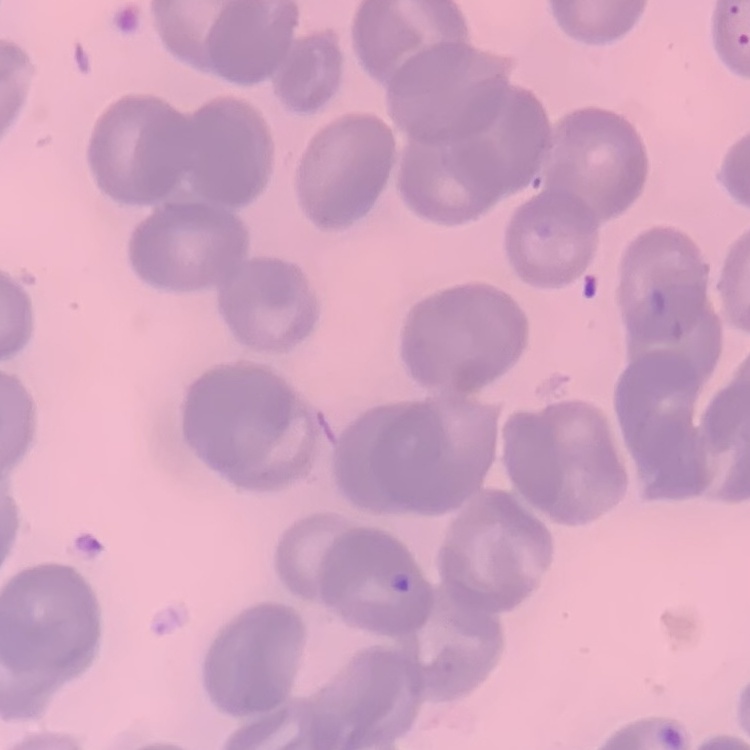
Summary:
  - Erythrocyte morphology: no rouleaux formation
  - Stain: Field's or Giemsa
  - Image type: square crop of a larger photomicrograph
  - Preparation: thin blood smear